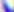
Summary:
  - Modality: micrograph
  - Magnification: 400x
  - Identification: Toxoplasma gondii